Assess the morphology of the red blood cells.
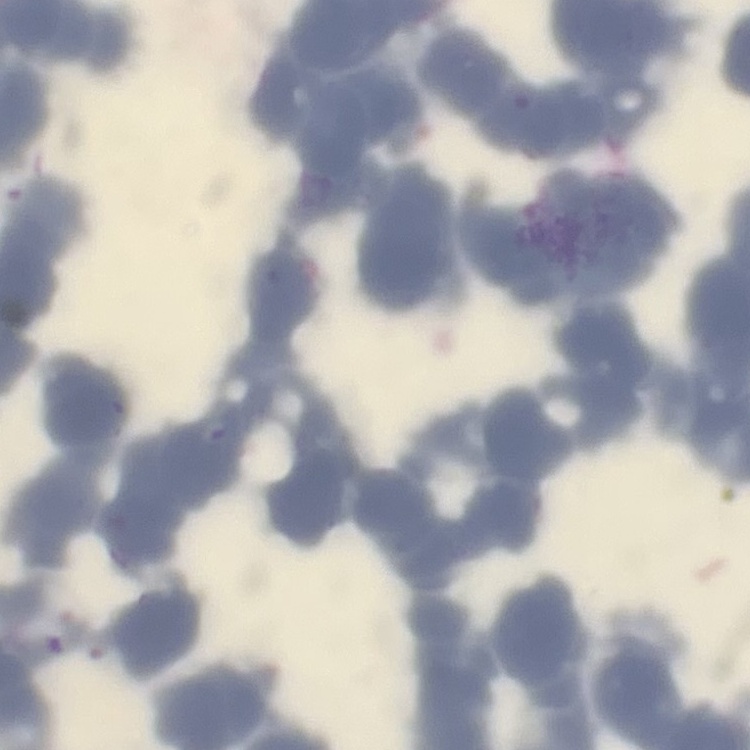

Rouleaux formation.

Square crop of a larger photomicrograph. Thin peripheral smear. Stained with either Field's or Giemsa.